Report the malaria status of this cell.
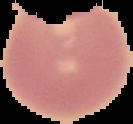
It is uninfected.

image type = cell region segmented out of the field of view; surrounding area masked to black
image size = 133×124 pixels
preparation = thin blood film